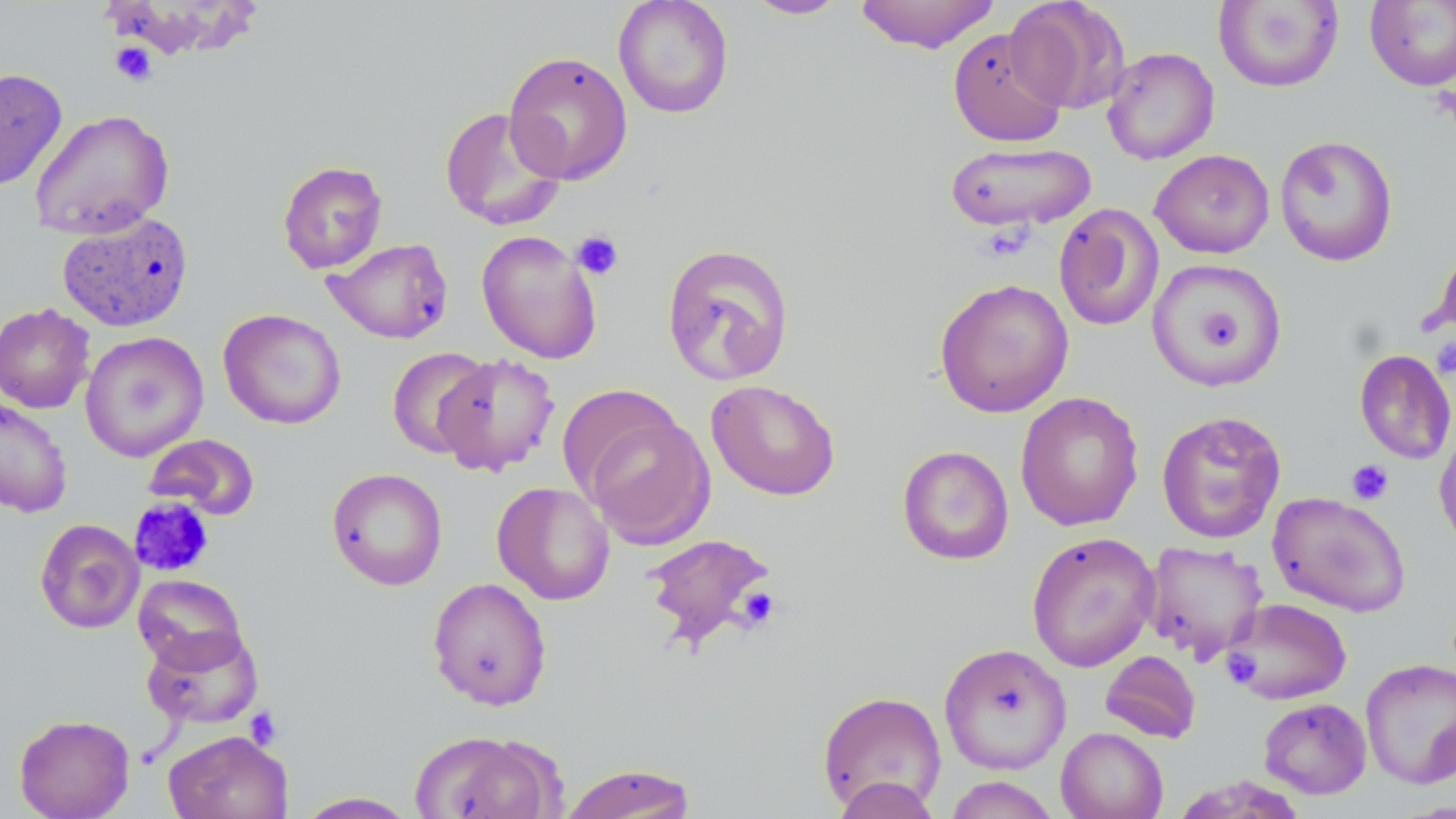

Summary:
  - Coordinate format: approximate bounding boxes as [x1, y1, x2, y2] in pixels
  - Platelet locations: [109, 41, 157, 86], [571, 230, 624, 281], [1431, 338, 1456, 378], [1346, 459, 1393, 505], [129, 497, 215, 577], [737, 586, 782, 630], [1221, 650, 1262, 690], [242, 707, 283, 749]
  - Uninfected red blood cell locations: [613, 0, 734, 119], [742, 0, 851, 20], [854, 0, 1001, 53], [1006, 1, 1131, 113], [1213, 1, 1344, 92], [1364, 1, 1456, 91], [948, 28, 1067, 147], [1102, 46, 1219, 165], [503, 51, 633, 185], [0, 67, 68, 191], [437, 106, 568, 231], [29, 109, 175, 240], [1274, 135, 1398, 267], [945, 141, 1097, 233], [1150, 149, 1275, 259], [277, 160, 388, 274], [1052, 203, 1165, 331], [57, 210, 194, 332], [477, 230, 602, 364], [322, 237, 454, 344], [661, 243, 796, 387], [1147, 258, 1288, 390], [934, 277, 1073, 418], [0, 302, 95, 414], [218, 308, 346, 430], [80, 331, 209, 462], [386, 347, 492, 459], [1354, 348, 1455, 464], [434, 352, 560, 476], [706, 379, 840, 501], [1015, 391, 1144, 531], [0, 396, 73, 517], [1156, 410, 1287, 544], [582, 412, 716, 549], [1434, 424, 1456, 555], [143, 433, 261, 521], [897, 445, 1014, 565], [326, 468, 448, 590], [492, 481, 615, 605], [1267, 491, 1412, 617], [35, 518, 144, 634], [1026, 531, 1160, 673], [643, 532, 778, 649], [1141, 540, 1268, 662], [133, 574, 248, 671], [427, 577, 552, 711], [1222, 597, 1352, 705], [142, 626, 263, 729], [938, 642, 1071, 774], [1100, 650, 1201, 744], [1360, 658, 1456, 789], [816, 690, 947, 814], [1258, 697, 1372, 799], [13, 713, 135, 819], [1056, 727, 1168, 819], [163, 729, 293, 819], [410, 729, 559, 819], [558, 762, 698, 818], [832, 776, 941, 818], [942, 776, 1062, 818], [1170, 776, 1312, 818], [293, 791, 422, 818]
  - Slide-level diagnosis: no evidence of blood parasites
  - Modality: optical microscopy
  - Preparation: thin blood smear
  - Magnification: 1000x
  - Field of view: one of a larger specimen
  - Image size: 1456×819 pixels
  - Stain: May-Grünwald-Giemsa